Classify this cell by malaria status.
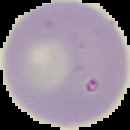

Uninfected.

From a thin blood smear. Image is 130×130 pixels. Segmented cell region on a black background.